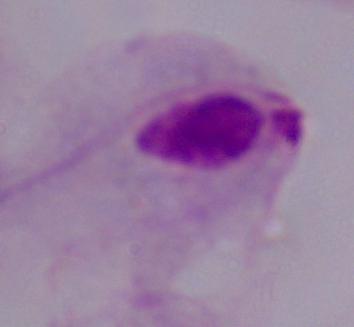

modality = micrograph
identification = trichomonad
magnification = 1000x